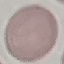

malaria status = uninfected
capture = smartphone camera at the microscope eyepiece
image type = automatically extracted cell patch, resized to 64 × 64 pixels
preparation = thin blood smear
stain = Giemsa